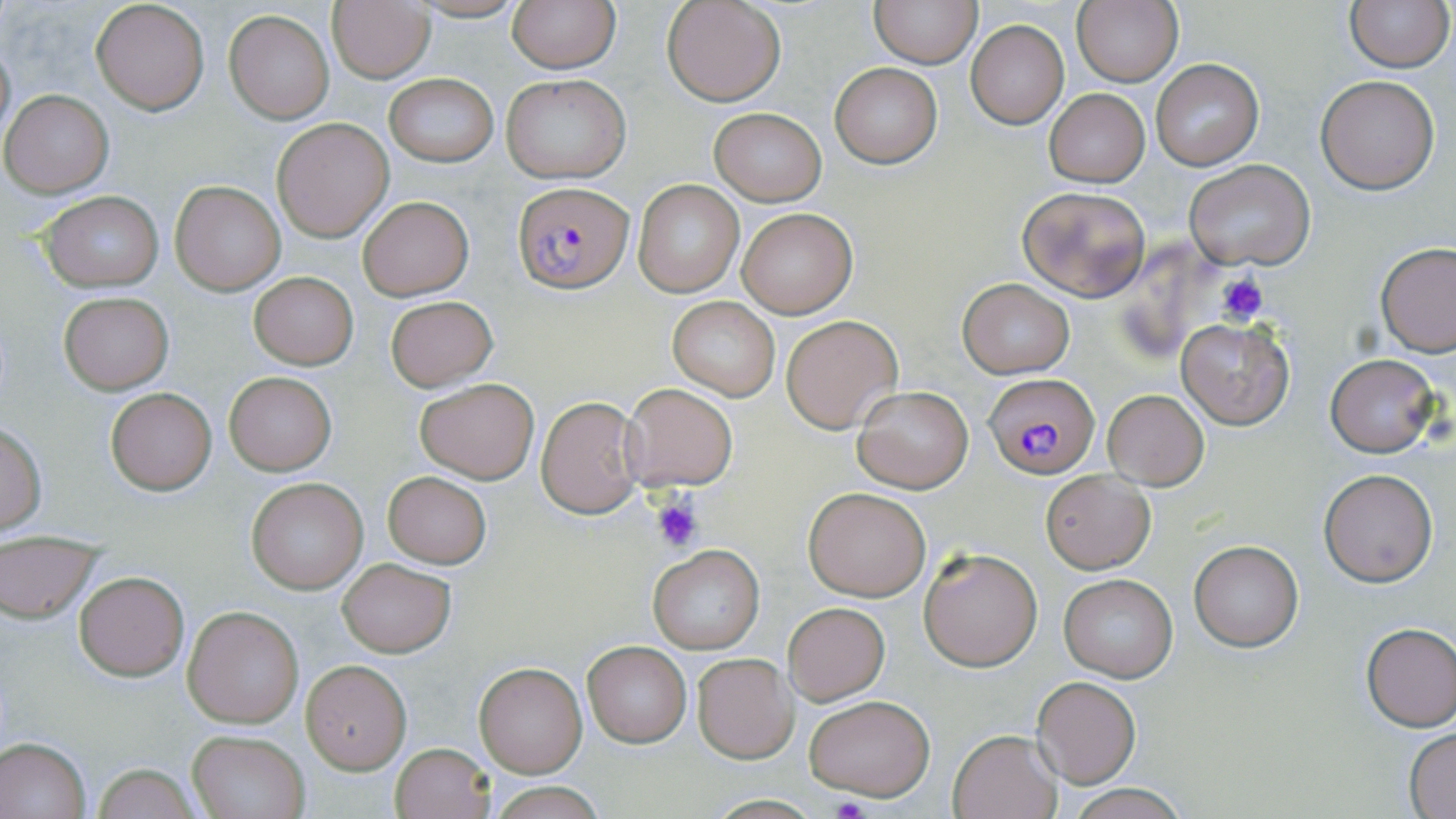
Summary:
  - Coordinate format: approximate bounding boxes as named x1/y1/x2/y2 corners in pixels
  - Platelet locations: (x1=1217, y1=275, x2=1267, y2=325), (x1=650, y1=494, x2=704, y2=552), (x1=831, y1=797, x2=870, y2=819)
  - Uninfected red blood cell locations: (x1=91, y1=0, x2=210, y2=115), (x1=404, y1=0, x2=532, y2=23), (x1=507, y1=0, x2=619, y2=72), (x1=661, y1=0, x2=786, y2=106), (x1=870, y1=0, x2=980, y2=68), (x1=1343, y1=0, x2=1452, y2=72), (x1=1071, y1=1, x2=1182, y2=88), (x1=328, y1=3, x2=434, y2=83), (x1=224, y1=10, x2=334, y2=123), (x1=965, y1=20, x2=1070, y2=129), (x1=0, y1=33, x2=16, y2=152), (x1=1151, y1=59, x2=1263, y2=169), (x1=830, y1=63, x2=942, y2=167), (x1=383, y1=73, x2=500, y2=167), (x1=501, y1=74, x2=630, y2=184), (x1=1316, y1=75, x2=1440, y2=193), (x1=1045, y1=89, x2=1149, y2=187), (x1=3, y1=90, x2=114, y2=197), (x1=709, y1=108, x2=826, y2=205), (x1=272, y1=118, x2=393, y2=241), (x1=1184, y1=161, x2=1314, y2=270), (x1=169, y1=179, x2=286, y2=296), (x1=632, y1=180, x2=745, y2=298), (x1=1016, y1=185, x2=1151, y2=301), (x1=38, y1=191, x2=163, y2=291), (x1=359, y1=196, x2=473, y2=300), (x1=737, y1=207, x2=857, y2=318), (x1=1376, y1=243, x2=1456, y2=358), (x1=249, y1=272, x2=359, y2=369), (x1=957, y1=278, x2=1075, y2=379), (x1=58, y1=291, x2=174, y2=394), (x1=384, y1=295, x2=498, y2=392), (x1=667, y1=295, x2=781, y2=402), (x1=781, y1=314, x2=903, y2=433), (x1=1176, y1=319, x2=1296, y2=430), (x1=1326, y1=353, x2=1440, y2=457), (x1=226, y1=372, x2=335, y2=474), (x1=414, y1=378, x2=539, y2=484), (x1=622, y1=382, x2=740, y2=493), (x1=853, y1=386, x2=973, y2=493), (x1=104, y1=387, x2=217, y2=494), (x1=1103, y1=390, x2=1209, y2=489), (x1=535, y1=394, x2=646, y2=519), (x1=0, y1=421, x2=48, y2=536), (x1=1319, y1=467, x2=1439, y2=587), (x1=1040, y1=469, x2=1155, y2=574), (x1=383, y1=472, x2=492, y2=569), (x1=246, y1=478, x2=367, y2=593), (x1=804, y1=485, x2=931, y2=601), (x1=0, y1=539, x2=102, y2=622), (x1=1189, y1=541, x2=1303, y2=652), (x1=648, y1=543, x2=763, y2=655), (x1=919, y1=547, x2=1043, y2=672), (x1=337, y1=559, x2=455, y2=658), (x1=74, y1=572, x2=189, y2=681), (x1=1059, y1=574, x2=1178, y2=682), (x1=783, y1=603, x2=890, y2=706), (x1=184, y1=606, x2=303, y2=728), (x1=1359, y1=622, x2=1456, y2=731), (x1=582, y1=642, x2=690, y2=747), (x1=691, y1=653, x2=798, y2=763), (x1=301, y1=660, x2=410, y2=773), (x1=474, y1=662, x2=587, y2=777), (x1=1030, y1=677, x2=1142, y2=789), (x1=804, y1=693, x2=935, y2=801), (x1=1405, y1=728, x2=1456, y2=817), (x1=947, y1=729, x2=1061, y2=818), (x1=188, y1=730, x2=308, y2=818), (x1=0, y1=735, x2=92, y2=818), (x1=389, y1=742, x2=495, y2=819), (x1=91, y1=764, x2=202, y2=819)
  - Plasmodium falciparum-infected red blood cell locations: (x1=513, y1=183, x2=634, y2=292), (x1=985, y1=374, x2=1099, y2=477)
  - Slide-level diagnosis: Plasmodium falciparum
  - Modality: light microscopy
  - Preparation: thin blood smear
  - Magnification: 1000x
  - Stain: May-Grünwald-Giemsa
  - Field of view: single
  - Image size: 1456×819 pixels